Locate every Trypanosoma brucei.
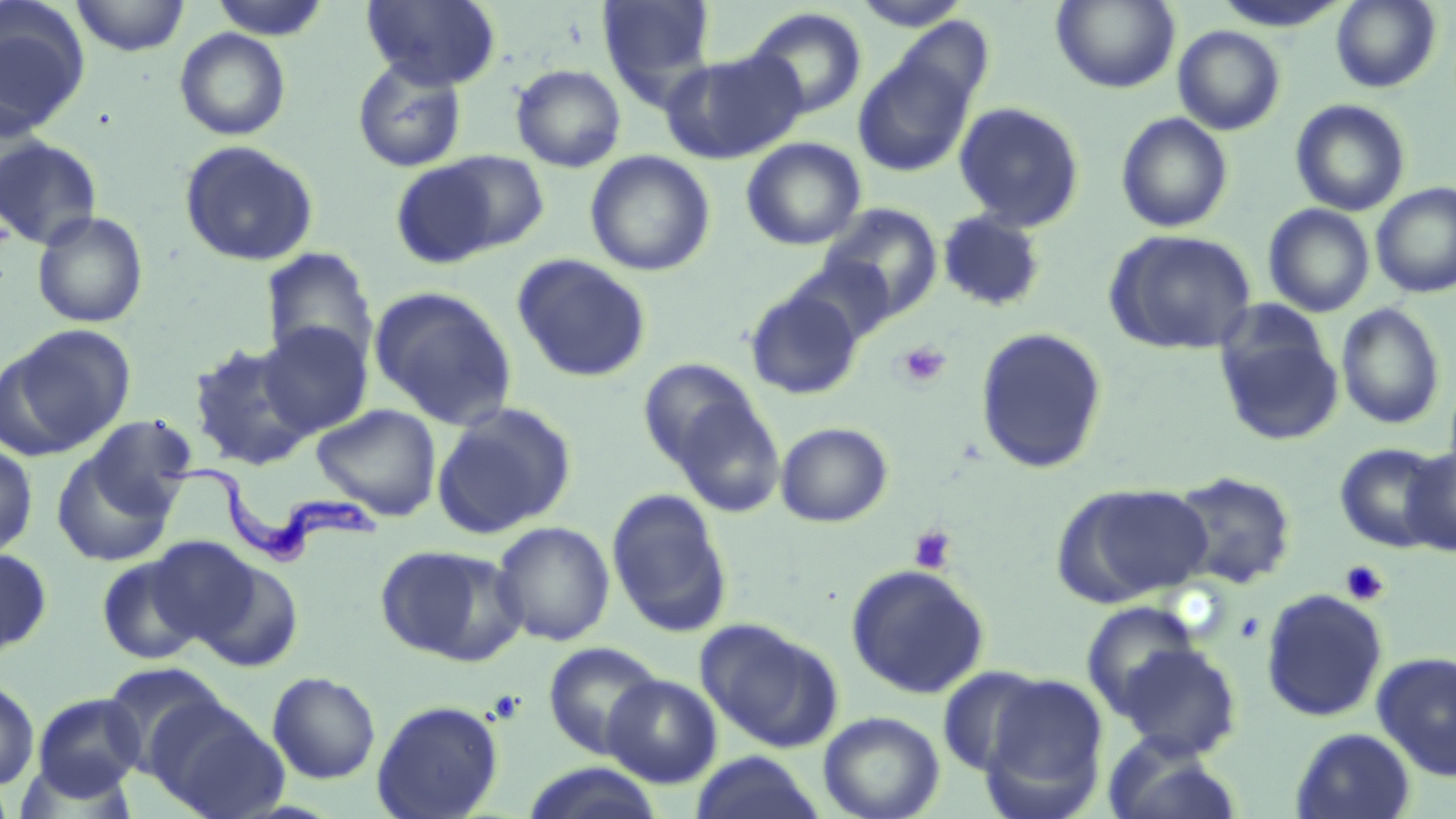

Approximate bounding boxes as [x1, y1, x2, y2] in pixels.
Trypanosoma brucei: [149, 452, 386, 565].

Platelet locations: [894, 341, 951, 389], [909, 526, 956, 574], [1339, 560, 1390, 606], [1234, 610, 1265, 644]. Uninfected red blood cell locations: [71, 0, 190, 56], [209, 0, 330, 40], [362, 0, 501, 90], [597, 0, 718, 102], [851, 0, 972, 31], [1052, 0, 1180, 92], [1331, 0, 1442, 93], [0, 5, 90, 138], [744, 6, 868, 121], [1173, 25, 1286, 135], [175, 28, 291, 141], [660, 50, 806, 164], [854, 54, 976, 176], [352, 58, 467, 173], [510, 63, 626, 172], [1290, 100, 1411, 216], [953, 102, 1085, 232], [1116, 112, 1233, 233], [0, 135, 103, 250], [742, 137, 866, 250], [179, 140, 319, 268], [436, 149, 552, 253], [585, 151, 715, 276], [389, 161, 503, 270], [1372, 183, 1456, 297], [820, 203, 944, 320], [1263, 204, 1375, 317], [937, 210, 1047, 312], [31, 211, 148, 328], [1104, 229, 1257, 355], [260, 248, 378, 368], [512, 254, 652, 383], [786, 256, 897, 347], [369, 286, 518, 429], [744, 288, 864, 400], [1336, 303, 1446, 430], [1214, 316, 1344, 447], [257, 321, 373, 436], [3, 324, 136, 455], [974, 326, 1109, 474], [187, 341, 316, 471], [638, 357, 763, 471], [668, 394, 786, 519], [432, 402, 576, 539], [311, 403, 442, 521], [81, 415, 199, 522], [775, 421, 893, 527], [1334, 442, 1448, 552], [0, 443, 38, 560], [50, 444, 180, 568], [1401, 446, 1456, 556], [1168, 470, 1297, 591], [1056, 482, 1215, 605], [606, 488, 733, 638], [491, 521, 615, 646], [145, 537, 261, 646], [375, 543, 524, 666], [0, 547, 52, 657], [96, 554, 206, 666], [193, 559, 304, 673], [846, 564, 990, 699], [1260, 588, 1388, 722], [1080, 601, 1201, 719], [696, 619, 840, 752], [542, 641, 665, 758], [1116, 642, 1242, 759], [1372, 651, 1456, 781], [100, 662, 230, 775], [935, 665, 1051, 778], [267, 671, 381, 784], [978, 672, 1110, 816], [603, 673, 722, 788], [0, 678, 39, 791], [32, 693, 146, 799], [148, 697, 289, 819], [371, 699, 505, 819], [818, 710, 945, 819], [1291, 727, 1416, 818], [1102, 734, 1244, 819], [688, 751, 827, 819], [520, 762, 667, 819]. Slide-level diagnosis: Trypanosoma brucei. Thin blood film. Captured at 1000x magnification. Single field of view. Optical microscopy. Image is 1456×819 pixels. May-Grünwald-Giemsa-stained preparation.